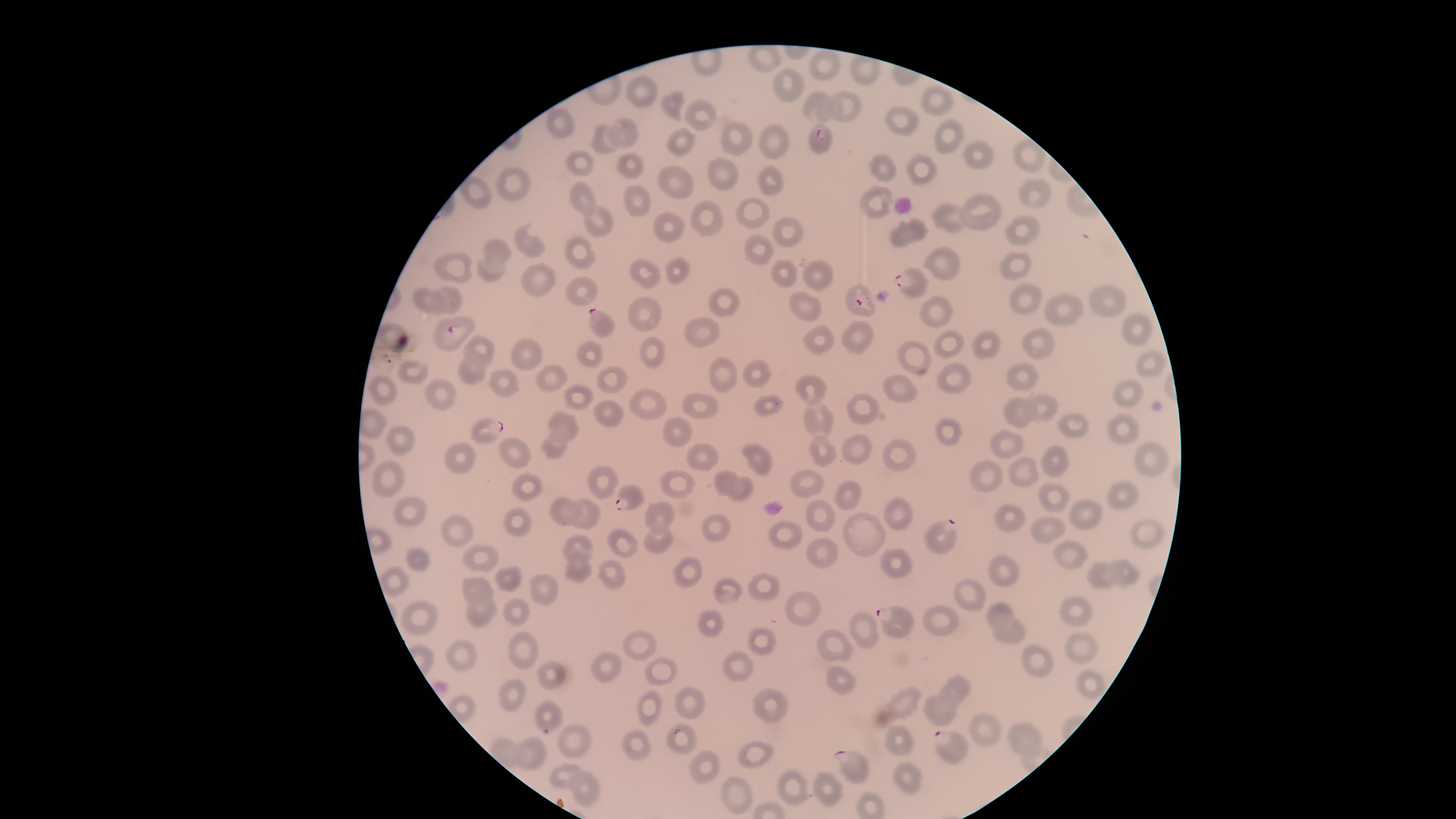

parasitized red blood cells = approximate bounding boxes, in pixels from the top-left corner: (left=809, top=124, right=834, bottom=154), (left=893, top=267, right=929, bottom=298), (left=845, top=283, right=877, bottom=317), (left=588, top=308, right=615, bottom=338), (left=432, top=316, right=476, bottom=352), (left=469, top=417, right=504, bottom=445), (left=614, top=484, right=644, bottom=511), (left=923, top=518, right=958, bottom=554), (left=876, top=605, right=914, bottom=638), (left=934, top=730, right=970, bottom=766), (left=834, top=750, right=870, bottom=784)
species = Plasmodium falciparum
visible region = circular
uninfected red blood cells = approximate bounding boxes, in pixels from the top-left corner: (left=808, top=49, right=841, bottom=82), (left=848, top=54, right=882, bottom=86), (left=770, top=67, right=805, bottom=104), (left=626, top=74, right=659, bottom=108), (left=920, top=83, right=954, bottom=117), (left=660, top=90, right=686, bottom=123), (left=801, top=90, right=837, bottom=125), (left=823, top=90, right=862, bottom=123), (left=684, top=99, right=718, bottom=131), (left=884, top=105, right=919, bottom=137), (left=605, top=117, right=639, bottom=148), (left=933, top=118, right=965, bottom=154), (left=721, top=122, right=753, bottom=156), (left=589, top=124, right=619, bottom=155), (left=758, top=124, right=791, bottom=159), (left=665, top=126, right=696, bottom=158), (left=1013, top=137, right=1046, bottom=174), (left=963, top=139, right=994, bottom=170), (left=565, top=149, right=594, bottom=177), (left=616, top=152, right=644, bottom=180), (left=868, top=153, right=897, bottom=182), (left=905, top=153, right=938, bottom=186), (left=707, top=156, right=740, bottom=192), (left=758, top=164, right=784, bottom=197), (left=656, top=165, right=696, bottom=199), (left=496, top=167, right=530, bottom=202), (left=459, top=174, right=493, bottom=209), (left=1018, top=177, right=1052, bottom=209), (left=569, top=181, right=596, bottom=216), (left=624, top=184, right=652, bottom=217), (left=859, top=186, right=894, bottom=220), (left=958, top=193, right=1003, bottom=232), (left=735, top=197, right=770, bottom=229), (left=689, top=199, right=724, bottom=237), (left=931, top=203, right=967, bottom=234), (left=582, top=204, right=614, bottom=238), (left=652, top=212, right=685, bottom=243), (left=1004, top=214, right=1041, bottom=247), (left=772, top=216, right=803, bottom=247), (left=889, top=218, right=929, bottom=248), (left=513, top=223, right=546, bottom=258), (left=744, top=234, right=775, bottom=265), (left=564, top=235, right=597, bottom=270), (left=482, top=237, right=512, bottom=273), (left=922, top=247, right=961, bottom=283), (left=999, top=251, right=1033, bottom=280), (left=433, top=252, right=472, bottom=283), (left=628, top=256, right=662, bottom=289), (left=664, top=256, right=690, bottom=285), (left=477, top=257, right=507, bottom=283), (left=770, top=260, right=798, bottom=287), (left=802, top=260, right=834, bottom=292), (left=520, top=263, right=557, bottom=298), (left=564, top=276, right=598, bottom=306), (left=1009, top=283, right=1042, bottom=315), (left=1089, top=283, right=1128, bottom=316), (left=432, top=286, right=462, bottom=315), (left=411, top=287, right=447, bottom=315), (left=708, top=287, right=740, bottom=318), (left=789, top=290, right=823, bottom=321), (left=1044, top=294, right=1085, bottom=326), (left=919, top=295, right=953, bottom=328), (left=628, top=296, right=662, bottom=332), (left=1121, top=314, right=1153, bottom=348), (left=683, top=316, right=720, bottom=348), (left=841, top=320, right=874, bottom=355), (left=375, top=321, right=408, bottom=353), (left=803, top=324, right=835, bottom=357), (left=1021, top=328, right=1054, bottom=359), (left=933, top=329, right=965, bottom=358), (left=971, top=330, right=1002, bottom=360), (left=463, top=335, right=494, bottom=368), (left=639, top=336, right=665, bottom=369), (left=510, top=338, right=544, bottom=370), (left=577, top=339, right=604, bottom=368), (left=895, top=340, right=932, bottom=376), (left=1135, top=351, right=1166, bottom=378), (left=457, top=356, right=485, bottom=387), (left=708, top=356, right=737, bottom=392), (left=396, top=359, right=430, bottom=386), (left=742, top=360, right=772, bottom=388), (left=936, top=362, right=972, bottom=395), (left=1004, top=362, right=1040, bottom=391), (left=535, top=364, right=568, bottom=393), (left=596, top=365, right=628, bottom=395), (left=489, top=369, right=521, bottom=398), (left=367, top=374, right=399, bottom=406), (left=883, top=374, right=919, bottom=403), (left=795, top=375, right=827, bottom=406), (left=424, top=378, right=457, bottom=411), (left=1112, top=378, right=1144, bottom=409), (left=563, top=385, right=594, bottom=410), (left=629, top=388, right=668, bottom=421), (left=681, top=392, right=719, bottom=419), (left=1024, top=392, right=1058, bottom=422), (left=846, top=393, right=880, bottom=426), (left=752, top=394, right=785, bottom=417), (left=1002, top=397, right=1037, bottom=429), (left=593, top=398, right=625, bottom=428), (left=803, top=400, right=833, bottom=440), (left=547, top=411, right=579, bottom=445), (left=1057, top=413, right=1090, bottom=439), (left=1108, top=413, right=1140, bottom=446), (left=662, top=417, right=693, bottom=447), (left=935, top=417, right=962, bottom=446), (left=385, top=425, right=416, bottom=456), (left=989, top=429, right=1025, bottom=459), (left=540, top=434, right=567, bottom=460), (left=809, top=434, right=837, bottom=469), (left=840, top=434, right=872, bottom=464), (left=499, top=436, right=532, bottom=469), (left=881, top=439, right=916, bottom=472), (left=1133, top=440, right=1168, bottom=478), (left=685, top=442, right=720, bottom=471), (left=445, top=443, right=476, bottom=474), (left=741, top=444, right=772, bottom=476), (left=1040, top=445, right=1070, bottom=476), (left=1007, top=456, right=1039, bottom=488), (left=371, top=460, right=404, bottom=498), (left=968, top=460, right=1003, bottom=492), (left=587, top=465, right=619, bottom=500), (left=659, top=469, right=695, bottom=499), (left=789, top=469, right=823, bottom=498), (left=713, top=470, right=739, bottom=497), (left=511, top=473, right=543, bottom=501), (left=727, top=476, right=753, bottom=501), (left=834, top=479, right=861, bottom=511), (left=1106, top=480, right=1141, bottom=511), (left=1037, top=482, right=1070, bottom=513), (left=394, top=496, right=429, bottom=526), (left=549, top=496, right=582, bottom=527), (left=883, top=497, right=914, bottom=530), (left=569, top=498, right=601, bottom=530), (left=806, top=499, right=836, bottom=532), (left=1067, top=499, right=1102, bottom=531), (left=644, top=500, right=676, bottom=537), (left=994, top=505, right=1025, bottom=532), (left=502, top=507, right=532, bottom=537), (left=842, top=511, right=886, bottom=558), (left=440, top=514, right=476, bottom=547), (left=700, top=514, right=731, bottom=542), (left=1029, top=516, right=1065, bottom=544), (left=1129, top=518, right=1165, bottom=549), (left=767, top=520, right=803, bottom=550), (left=607, top=528, right=639, bottom=558), (left=644, top=528, right=673, bottom=553), (left=562, top=533, right=593, bottom=563), (left=806, top=537, right=839, bottom=569), (left=1053, top=540, right=1088, bottom=570), (left=462, top=544, right=499, bottom=573), (left=403, top=547, right=431, bottom=572), (left=881, top=548, right=913, bottom=580), (left=989, top=554, right=1021, bottom=587), (left=671, top=556, right=703, bottom=589), (left=563, top=558, right=593, bottom=583), (left=1107, top=558, right=1140, bottom=588), (left=597, top=559, right=627, bottom=590), (left=1087, top=562, right=1118, bottom=590), (left=494, top=565, right=521, bottom=592), (left=380, top=566, right=409, bottom=597), (left=746, top=571, right=781, bottom=602), (left=529, top=573, right=560, bottom=606), (left=460, top=577, right=494, bottom=606), (left=712, top=577, right=743, bottom=604), (left=952, top=578, right=988, bottom=612), (left=784, top=590, right=821, bottom=626), (left=1059, top=594, right=1093, bottom=627), (left=465, top=596, right=498, bottom=628), (left=502, top=598, right=531, bottom=628), (left=401, top=599, right=439, bottom=636), (left=985, top=601, right=1015, bottom=629), (left=921, top=605, right=960, bottom=637), (left=696, top=610, right=724, bottom=639), (left=848, top=610, right=879, bottom=651), (left=992, top=617, right=1026, bottom=645), (left=747, top=627, right=776, bottom=656), (left=621, top=629, right=657, bottom=662), (left=816, top=629, right=854, bottom=663), (left=507, top=631, right=539, bottom=670), (left=1064, top=631, right=1098, bottom=664), (left=446, top=639, right=479, bottom=673), (left=1021, top=644, right=1053, bottom=679), (left=591, top=650, right=623, bottom=683), (left=721, top=650, right=755, bottom=684), (left=643, top=656, right=678, bottom=687), (left=536, top=659, right=567, bottom=691), (left=826, top=665, right=856, bottom=694), (left=1075, top=668, right=1106, bottom=701), (left=939, top=674, right=972, bottom=707), (left=497, top=678, right=528, bottom=711), (left=883, top=686, right=922, bottom=722), (left=674, top=687, right=705, bottom=718), (left=752, top=688, right=789, bottom=724), (left=637, top=689, right=663, bottom=726), (left=922, top=693, right=956, bottom=727), (left=534, top=699, right=562, bottom=734), (left=968, top=712, right=1002, bottom=747), (left=1006, top=720, right=1043, bottom=759), (left=665, top=721, right=698, bottom=754), (left=557, top=722, right=592, bottom=759), (left=884, top=725, right=915, bottom=756), (left=621, top=728, right=654, bottom=761), (left=514, top=736, right=547, bottom=772), (left=736, top=739, right=776, bottom=770), (left=688, top=749, right=723, bottom=784), (left=891, top=762, right=923, bottom=796), (left=549, top=764, right=581, bottom=789), (left=776, top=769, right=809, bottom=806), (left=813, top=769, right=844, bottom=808), (left=567, top=772, right=601, bottom=808), (left=721, top=775, right=754, bottom=814)
stain = Giemsa
image size = 1456×819 pixels
presence = malaria parasites identified
preparation = thin blood smear
field of view = single
capture = smartphone photograph through the microscope eyepiece